Report the malaria status of this cell.
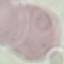

Uninfected.

Giemsa stain. Automatically extracted cell patch, resized to 64 × 64 pixels. Thin smear of blood. Photographed with a smartphone camera at the microscope eyepiece.